Outline each blood parasite and name the species.
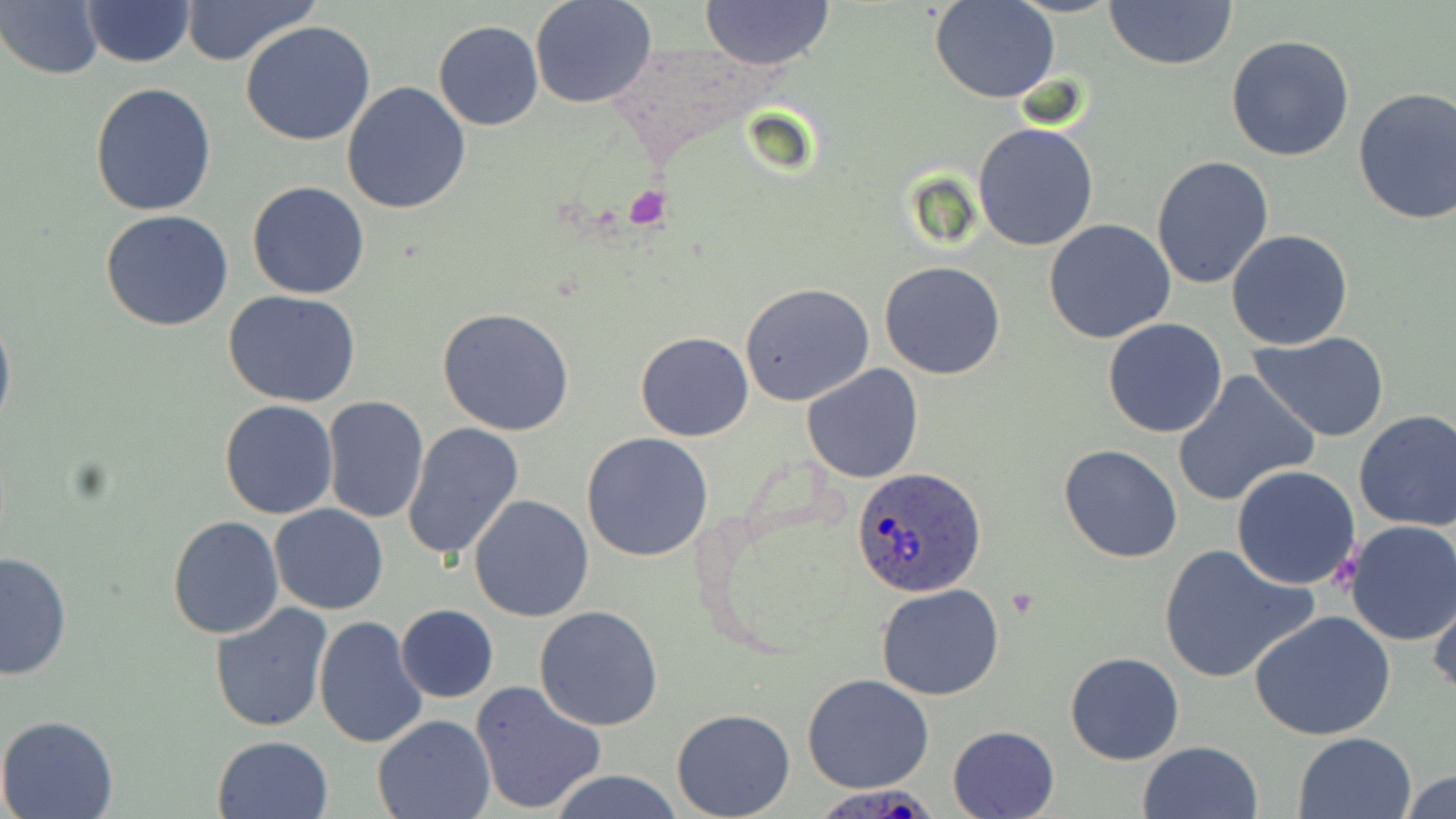
Approximate bounding boxes as [x1, y1, x2, y2] in pixels.
Plasmodium ovale-infected red blood cells: [851, 466, 987, 597], [813, 786, 943, 818].
No Plasmodium falciparum, Plasmodium malariae, Plasmodium vivax, Babesia divergens, or Trypanosoma brucei observed.

Uninfected red blood cell locations: [179, 0, 320, 67], [529, 0, 656, 109], [1103, 0, 1240, 71], [82, 1, 194, 68], [700, 1, 834, 69], [931, 1, 1057, 103], [2, 2, 103, 80], [241, 20, 376, 146], [433, 20, 543, 131], [1226, 34, 1355, 161], [90, 81, 218, 216], [341, 82, 472, 215], [1352, 86, 1456, 224], [972, 121, 1101, 251], [1151, 154, 1275, 290], [247, 181, 371, 299], [101, 208, 234, 331], [1043, 218, 1176, 344], [1226, 230, 1353, 351], [879, 262, 1006, 380], [740, 282, 876, 406], [222, 289, 361, 407], [439, 307, 574, 435], [0, 308, 15, 439], [1102, 318, 1229, 438], [635, 331, 754, 441], [1249, 331, 1393, 441], [1285, 348, 1436, 477], [801, 363, 924, 483], [1171, 369, 1319, 508], [321, 397, 429, 523], [219, 400, 339, 519], [1352, 410, 1456, 531], [402, 421, 524, 563], [581, 432, 713, 560], [1058, 445, 1184, 564], [1232, 464, 1362, 589], [468, 494, 593, 623], [269, 504, 390, 614], [167, 517, 284, 638], [1343, 521, 1456, 646], [1158, 544, 1318, 684], [0, 550, 71, 680], [1427, 580, 1456, 701], [876, 584, 1005, 700], [210, 602, 333, 733], [396, 605, 498, 702], [534, 605, 665, 732], [1248, 610, 1397, 742], [315, 615, 428, 748], [1064, 651, 1184, 765], [802, 673, 934, 792], [469, 680, 606, 815], [671, 709, 796, 819], [0, 715, 121, 819], [371, 715, 494, 819], [948, 725, 1059, 818], [1295, 732, 1419, 819], [212, 733, 334, 818], [1137, 740, 1263, 819], [546, 768, 685, 819], [1401, 769, 1456, 819]. Platelet locations: [622, 185, 670, 231], [1331, 550, 1360, 586]. Slide-level diagnosis: Plasmodium ovale. May-Grünwald-Giemsa-stained preparation. Light microscopy. Thin blood smear. Image is 1456×819 pixels. Captured at 1000x magnification. Single field of view.